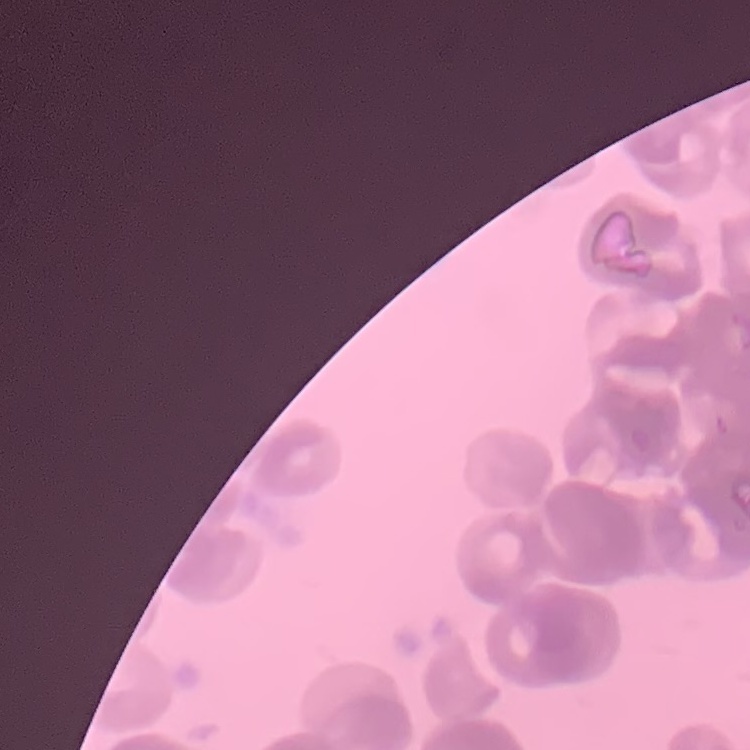
erythrocyte morphology = rouleaux formation
preparation = thin peripheral smear
stain = Field's or Giemsa
image type = square crop of a larger photomicrograph